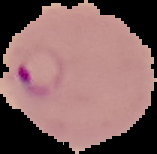

image size = 157×154 pixels
image type = cell region segmented out of the field of view; surrounding area masked to black
preparation = thin blood smear
result = malaria parasites detected